Locate platelets.
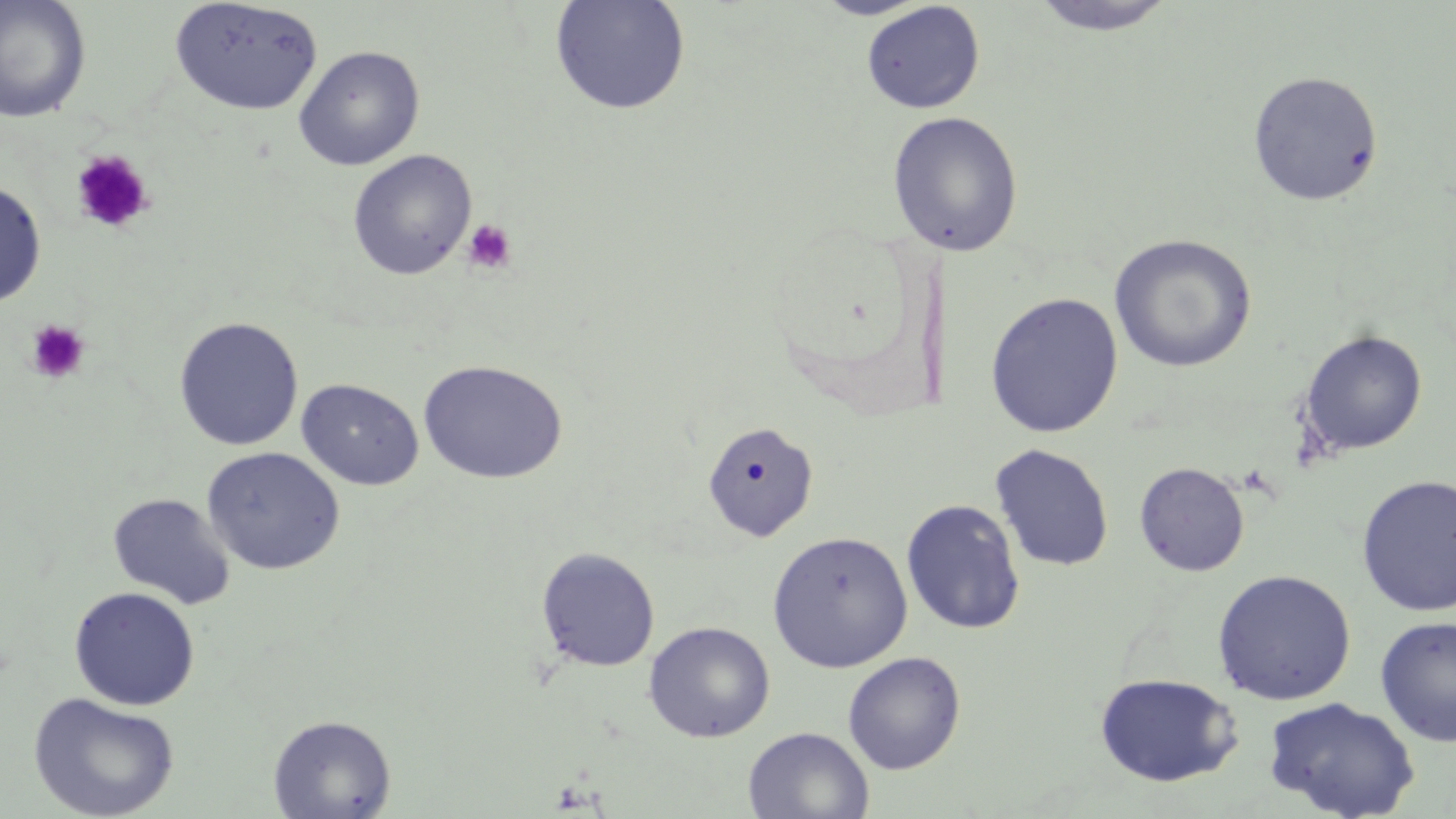
Approximate bounding boxes as (x1,y1)-(x2,y2) corner pairs in pixels.
Platelets: (70,149)-(154,234), (462,218)-(518,274), (25,319)-(90,385).

Uninfected red blood cell locations: (0,0)-(92,123), (549,0)-(692,116), (813,0)-(933,20), (1026,0)-(1179,36), (168,1)-(324,115), (860,2)-(985,114), (293,45)-(425,171), (1247,70)-(1384,206), (886,110)-(1024,257), (347,150)-(478,280), (0,180)-(47,308), (1109,234)-(1257,372), (984,293)-(1124,437), (173,316)-(304,451), (1298,328)-(1428,457), (418,359)-(568,484), (296,378)-(425,490), (701,421)-(818,541), (990,443)-(1114,572), (201,446)-(345,575), (1134,462)-(1250,576), (1356,474)-(1456,616), (107,492)-(235,610), (901,499)-(1026,635), (767,531)-(913,673), (535,546)-(660,672), (1211,569)-(1356,706), (68,586)-(200,710), (1374,615)-(1456,747), (643,621)-(775,743), (842,651)-(966,774), (1094,672)-(1243,787), (28,691)-(180,819), (1263,697)-(1420,819), (268,714)-(396,819), (743,726)-(874,818). Slide-level diagnosis: no evidence of blood parasites. Thin blood smear. May-Grünwald-Giemsa stain. Captured at 1000x magnification. Light microscopy. One field of a larger specimen. Image is 1456×819 pixels.